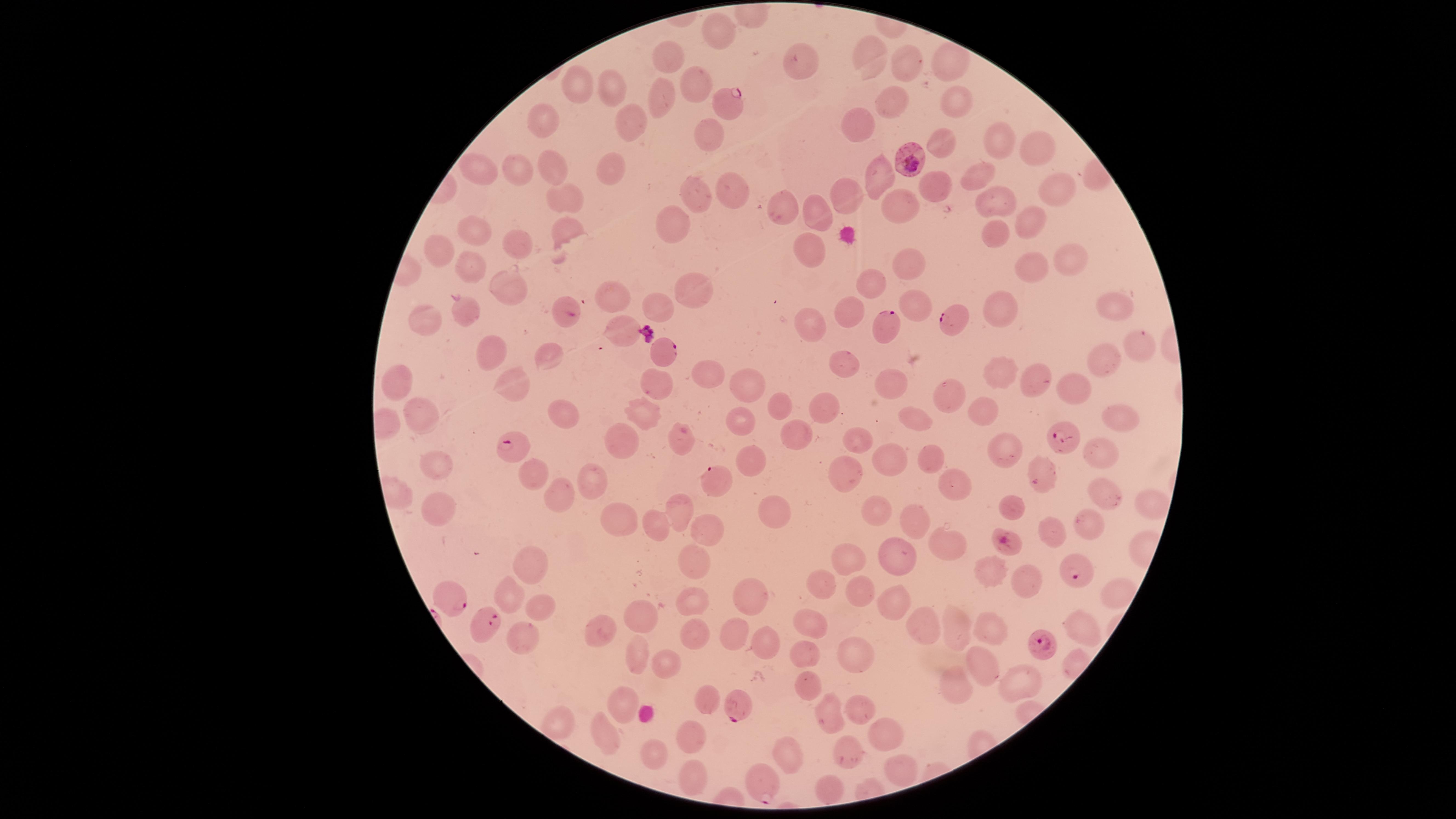
{
  "visible_region": "circular",
  "capture": "smartphone photograph through the microscope eyepiece",
  "parasitized_RBCs": "approximate marker points as (x, y) in pixels: (728, 98), (908, 158), (948, 317), (883, 324), (666, 354), (1061, 435), (520, 443), (713, 479), (999, 541), (1072, 572), (451, 597), (484, 624), (1044, 642), (739, 703), (763, 791)",
  "uninfected_RBCs": "approximate marker points as (x, y) in pixels: (721, 35), (866, 55), (670, 58), (802, 63), (905, 64), (949, 65), (692, 82), (579, 88), (608, 89), (657, 104), (959, 104), (894, 110), (859, 121), (541, 124), (630, 124), (706, 138), (943, 139), (996, 142), (1043, 148), (554, 167), (605, 170), (480, 174), (520, 174), (879, 177), (981, 179), (729, 187), (934, 188), (845, 189), (1057, 189), (990, 197), (564, 199), (698, 199), (903, 206), (783, 211), (819, 213), (1029, 222), (675, 225), (475, 233), (996, 233), (566, 234), (520, 247), (809, 254), (1067, 254), (442, 255), (1032, 258), (907, 261), (469, 268), (873, 282), (509, 286), (693, 288), (1006, 300), (655, 303), (616, 304), (915, 306), (1112, 307), (470, 312), (851, 312), (426, 315), (618, 326), (812, 326), (1131, 344), (483, 347), (548, 353), (1100, 359), (842, 360), (1000, 373), (703, 375), (401, 377), (1039, 377), (660, 380), (513, 384), (754, 384), (893, 384), (1076, 387), (943, 388), (779, 403), (826, 406), (984, 411), (565, 412), (425, 416), (911, 416), (638, 417), (1118, 417), (738, 418), (797, 425), (682, 436), (857, 438), (620, 443), (998, 449), (925, 452), (1101, 452), (752, 459), (895, 465), (435, 467), (535, 471), (838, 477), (1038, 480), (589, 481), (951, 483), (556, 495), (1100, 499), (680, 504), (435, 506), (1148, 506), (1017, 507), (878, 513), (775, 515), (612, 516), (1093, 521), (654, 525), (1053, 525), (915, 526), (710, 528), (633, 533), (944, 543), (899, 554), (850, 558), (693, 561), (533, 564), (991, 567), (1021, 579), (820, 583), (854, 589), (507, 593), (694, 594), (1114, 595), (752, 599), (543, 608), (895, 609), (641, 620), (809, 623), (927, 624), (958, 627), (1078, 627), (603, 631), (995, 632), (692, 633), (739, 633), (522, 636), (768, 641), (641, 654), (858, 655), (802, 656), (665, 664), (980, 665), (1019, 680), (806, 681), (955, 684), (708, 695), (619, 696), (857, 707), (831, 714), (558, 726), (885, 729), (605, 732), (695, 732), (1353, 737), (789, 751), (850, 752), (652, 753), (895, 770), (693, 773), (826, 788)",
  "preparation": "thin blood smear",
  "field_of_view": "single",
  "image_size": "1456×819 pixels",
  "presence": "malaria parasites seen",
  "stain": "Giemsa",
  "species": "Plasmodium falciparum"
}